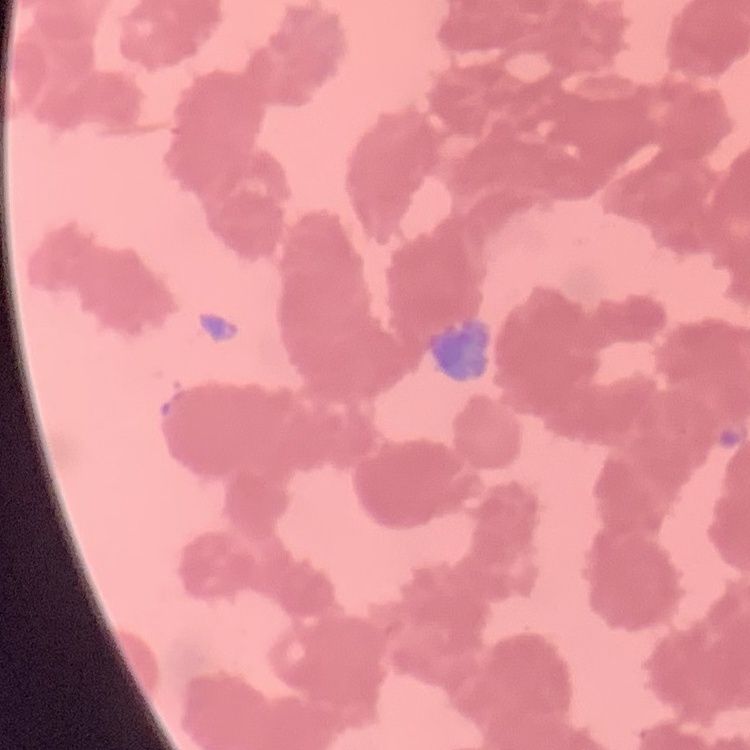

Summary:
  - Erythrocyte morphology: rouleaux formation
  - Stain: Field's or Giemsa
  - Image type: square crop of a larger photomicrograph
  - Preparation: thin peripheral smear